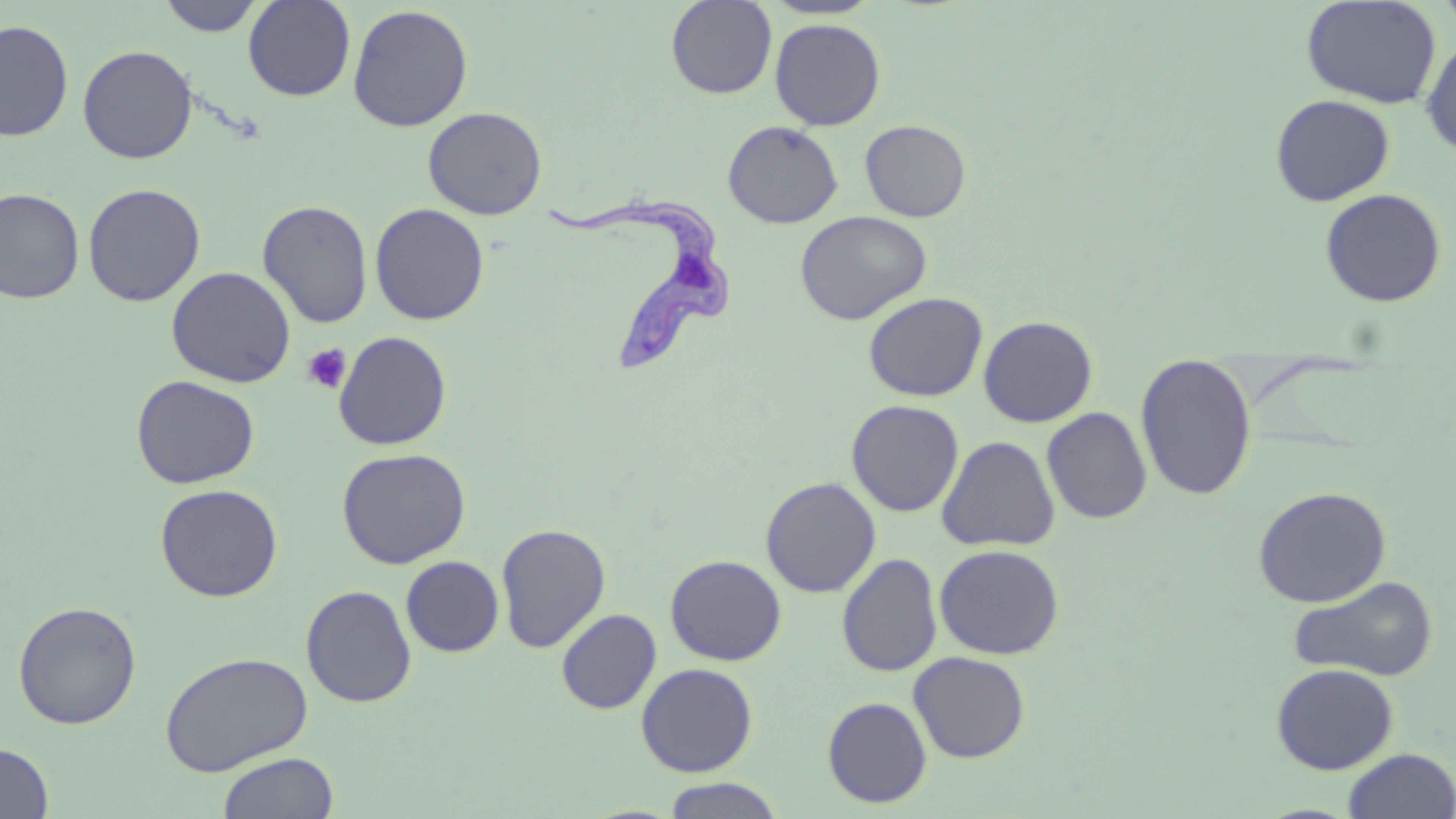

slide-level diagnosis = Trypanosoma brucei
modality = optical microscopy
field of view = one of a larger specimen
magnification = 1000x
stain = May-Grünwald-Giemsa
Trypanosoma brucei locations = approximate bounding boxes as [x1, y1, x2, y2] in pixels: [541, 192, 737, 374]
uninfected red blood cell locations = approximate bounding boxes as [x1, y1, x2, y2] in pixels: [157, 0, 266, 37], [243, 0, 355, 101], [666, 0, 777, 99], [761, 0, 884, 20], [1301, 0, 1441, 108], [348, 4, 473, 131], [0, 18, 74, 142], [770, 18, 886, 131], [1420, 34, 1456, 158], [78, 44, 198, 164], [1270, 94, 1395, 206], [423, 106, 548, 219], [723, 120, 843, 229], [860, 120, 970, 222], [83, 183, 206, 306], [0, 188, 85, 304], [1319, 188, 1447, 308], [257, 200, 373, 328], [370, 203, 490, 325], [795, 210, 932, 325], [166, 266, 296, 388], [863, 292, 988, 402], [864, 304, 1101, 412], [978, 315, 1098, 428], [334, 331, 452, 450], [1136, 354, 1257, 501], [131, 375, 260, 489], [846, 400, 964, 517], [1041, 407, 1152, 524], [936, 435, 1060, 552], [336, 447, 471, 569], [760, 477, 881, 598], [155, 483, 283, 602], [1253, 486, 1391, 607], [496, 522, 611, 653], [934, 544, 1064, 660], [837, 553, 942, 677], [665, 554, 787, 666], [401, 556, 504, 657], [1287, 575, 1439, 682], [301, 585, 417, 708], [12, 601, 142, 729], [556, 608, 661, 714], [160, 650, 313, 776], [908, 651, 1031, 763], [636, 662, 758, 777], [1271, 663, 1398, 775], [821, 696, 932, 808], [0, 742, 54, 819], [1342, 748, 1456, 819], [217, 752, 339, 819], [660, 778, 787, 818]
platelet locations = approximate bounding boxes as [x1, y1, x2, y2] in pixels: [302, 344, 352, 394]
image size = 1456×819 pixels
preparation = thin blood smear